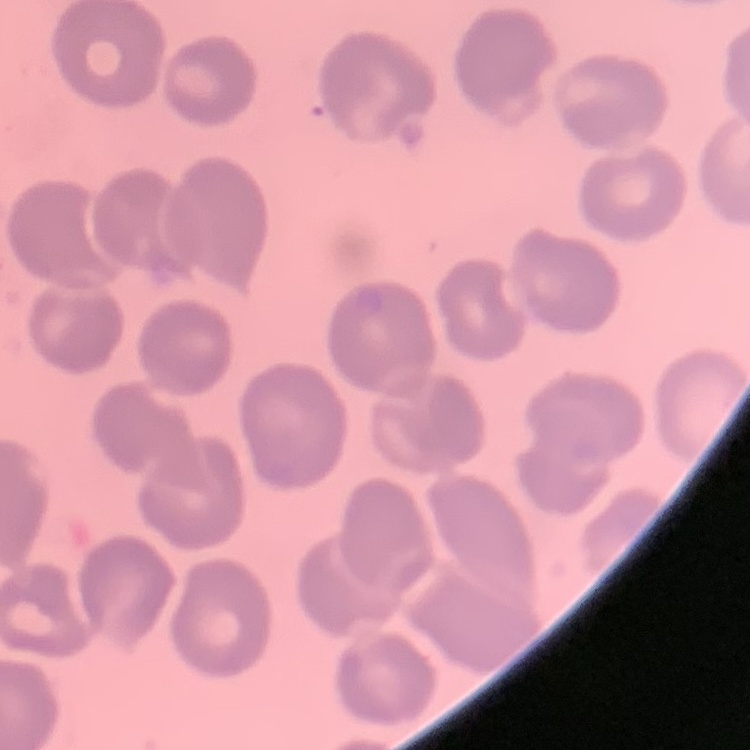
{
  "red_blood_cell_morphology": "no rouleaux formation",
  "stain": "Field's or Giemsa",
  "preparation": "thin blood smear",
  "image_type": "square crop of a larger photomicrograph"
}